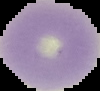

Image is 100×91 pixels. Result: no Plasmodium parasites detected. From a thin blood smear. Cell region segmented out of the field of view; the surrounding area is masked to black.